Report the malaria status of this cell.
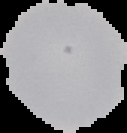
Uninfected.

The area outside the segmented cell region is set to black. Image is 127×133 pixels. From a thin blood smear.